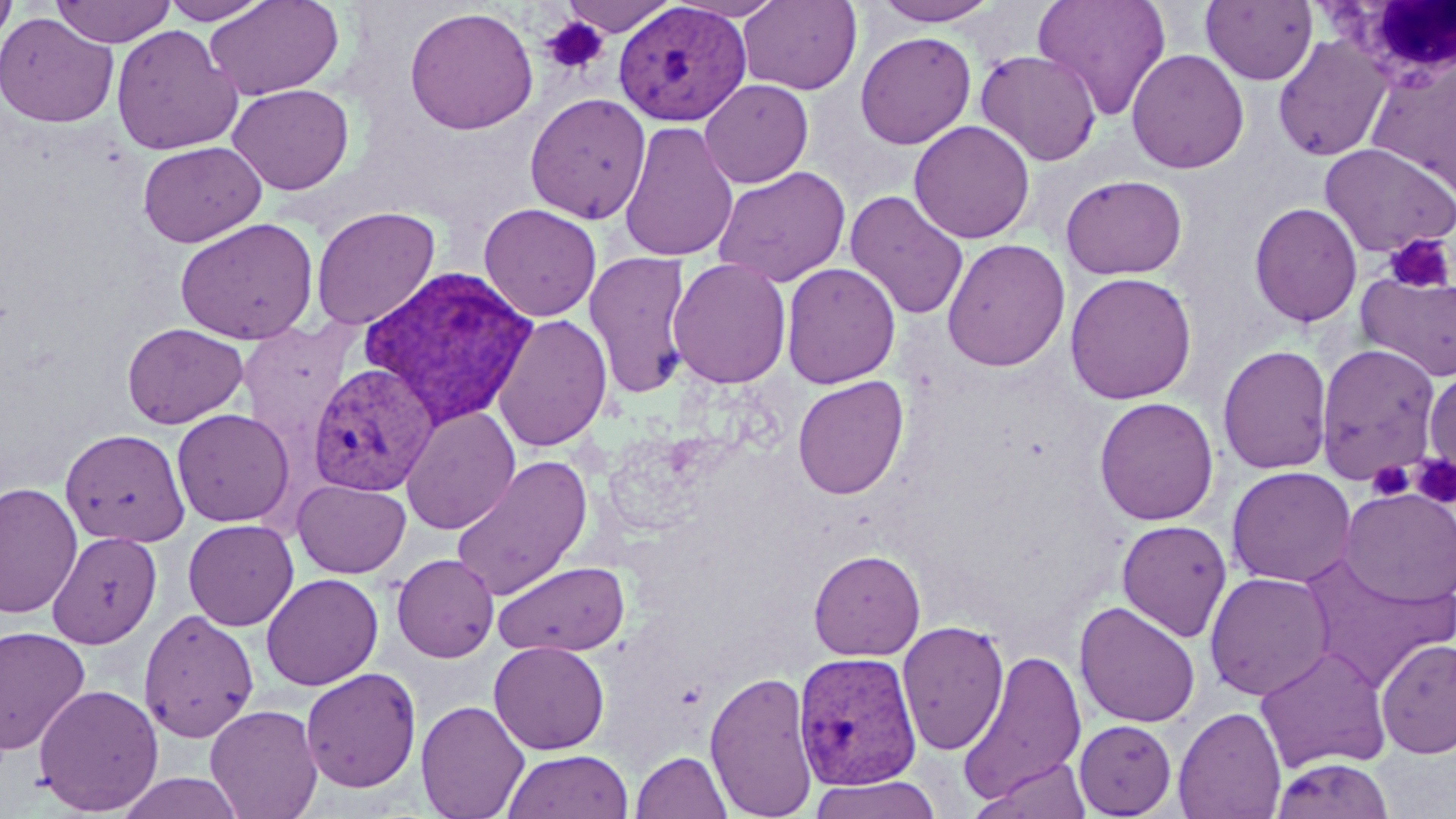

slide_level_diagnosis: Plasmodium vivax
uninfected_red_blood_cell_locations: 'approximate bounding boxes as [x1, y1, x2, y2] in pixels: [0, 0, 18, 50], [51, 0, 176, 47], [158, 0, 273, 25], [204, 0, 344, 100], [558, 0, 678, 36], [666, 0, 787, 21], [870, 0, 1003, 26], [1033, 0, 1171, 121], [738, 1, 862, 94], [1200, 1, 1318, 85], [404, 6, 539, 135], [0, 13, 119, 128], [110, 24, 243, 155], [855, 31, 977, 149], [1272, 36, 1393, 162], [855, 39, 1101, 156], [1126, 48, 1249, 174], [975, 49, 1102, 166], [700, 79, 813, 188], [228, 83, 354, 195], [524, 92, 651, 223], [909, 120, 1035, 244], [619, 121, 739, 263], [138, 141, 265, 247], [1318, 142, 1456, 257], [714, 166, 851, 288], [1060, 173, 1188, 279], [845, 190, 969, 321], [1249, 202, 1363, 327], [479, 203, 602, 321], [311, 206, 440, 331], [175, 217, 319, 344], [941, 238, 1070, 372], [584, 250, 692, 400], [667, 258, 792, 389], [781, 262, 901, 388], [1355, 271, 1456, 382], [1064, 272, 1197, 404], [492, 314, 613, 452], [236, 320, 362, 452], [122, 323, 248, 429], [1315, 343, 1442, 485], [1217, 344, 1333, 474], [1424, 367, 1456, 487], [792, 375, 909, 499], [1094, 397, 1219, 525], [400, 406, 520, 535], [171, 408, 294, 527], [60, 428, 190, 546], [450, 455, 592, 600], [1227, 466, 1357, 588], [292, 479, 411, 578], [0, 482, 82, 619], [1338, 488, 1456, 608], [183, 519, 299, 630], [1117, 519, 1233, 642], [47, 531, 163, 649], [808, 549, 925, 661], [1297, 552, 1454, 693], [392, 553, 499, 663], [493, 560, 630, 657], [1204, 571, 1335, 701], [261, 573, 383, 690], [1074, 601, 1200, 729], [139, 609, 260, 742], [896, 620, 1010, 756], [0, 625, 91, 754], [1375, 637, 1456, 759], [489, 641, 609, 754], [1255, 646, 1392, 774], [959, 650, 1088, 805], [300, 667, 421, 793], [705, 669, 819, 818], [33, 684, 164, 815], [416, 700, 529, 819], [205, 703, 323, 819], [1173, 705, 1287, 819], [1074, 719, 1177, 817], [503, 749, 633, 819], [630, 750, 732, 819], [972, 757, 1094, 818], [1270, 757, 1396, 819], [115, 773, 247, 819], [809, 775, 941, 819]'
plasmodium_vivax_infected_red_blood_cell_locations: 'approximate bounding boxes as [x1, y1, x2, y2] in pixels: [613, 1, 751, 126], [357, 265, 539, 430], [307, 363, 439, 497], [792, 650, 921, 791]'
image_size: 1456×819 pixels
white_blood_cell_locations: 'approximate bounding boxes as [x1, y1, x2, y2] in pixels: [1312, 1, 1456, 88]'
preparation: thin blood film
platelet_locations: 'approximate bounding boxes as [x1, y1, x2, y2] in pixels: [540, 16, 610, 76], [1384, 233, 1454, 294], [1412, 456, 1456, 509], [1367, 460, 1413, 501]'
stain: May-Grünwald-Giemsa
field_of_view: single
magnification: 1000x
modality: optical microscopy